Assess the morphology of the erythrocytes.
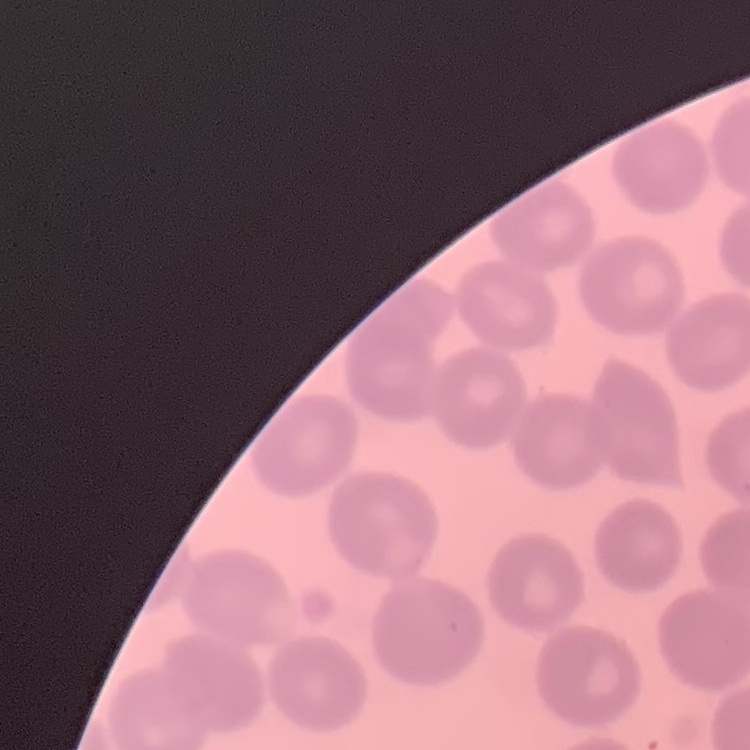
No rouleaux formation.

One tile cut from a larger photomicrograph. Thin blood smear. Stained with either Field's or Giemsa.